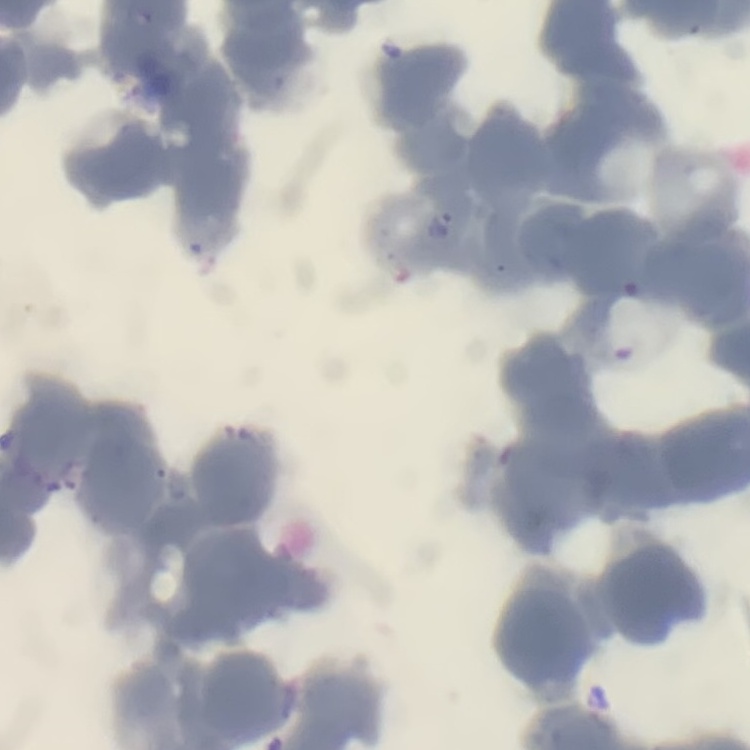

Summary:
  - Red blood cell morphology: rouleaux formation
  - Preparation: thin peripheral smear
  - Image type: square crop of a larger photomicrograph
  - Stain: Field's or Giemsa